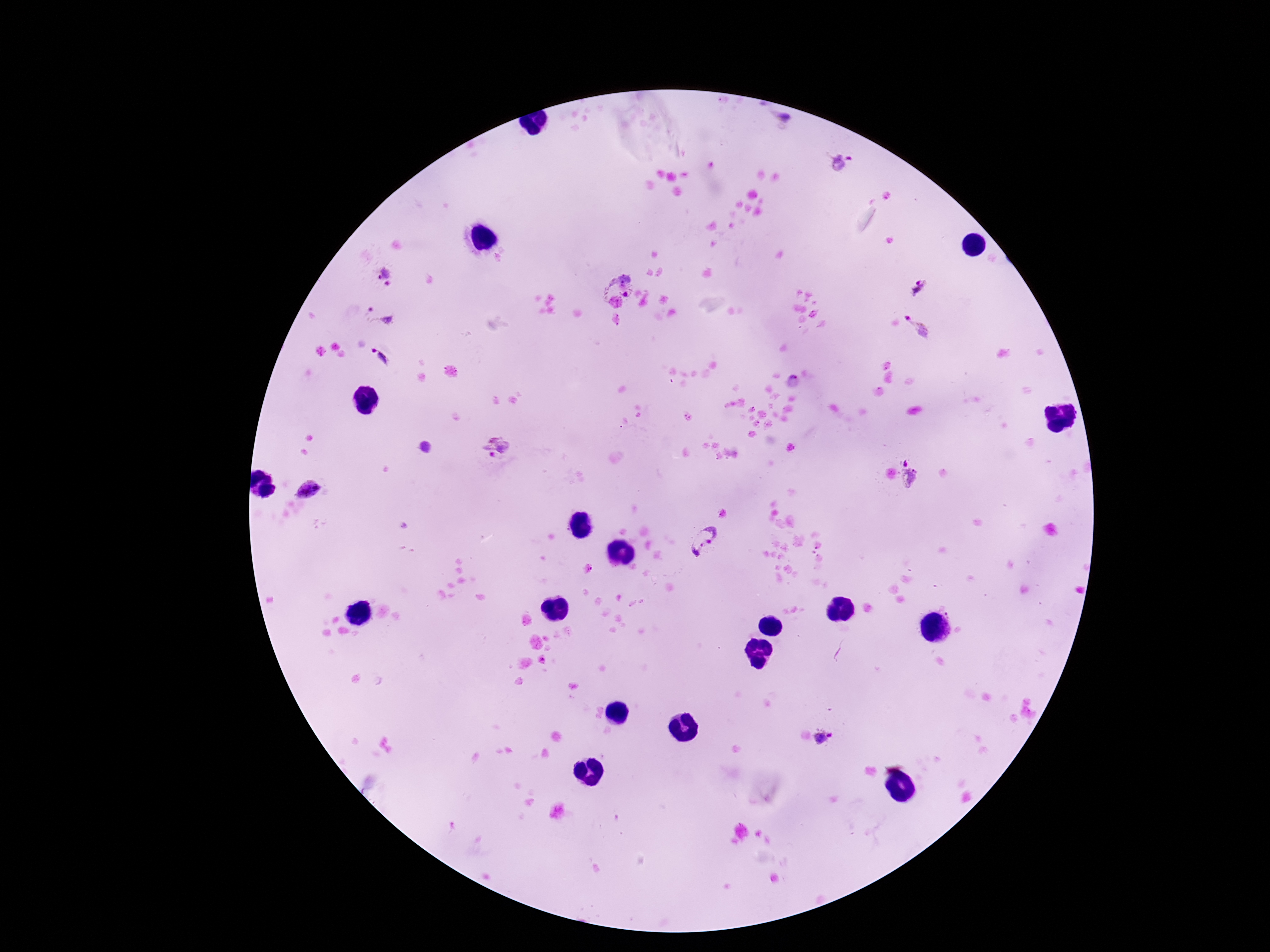
Approximate centers as [x, y] in pixels. Plasmodium parasite locations: [841, 163], [386, 276], [615, 278], [921, 287], [378, 315], [919, 326], [381, 356], [496, 448], [912, 473], [309, 490], [707, 543], [825, 737]. Smartphone photograph taken through the microscope eyepiece. Single field of view. 100x magnification. Image is 1270×952 pixels. Patient malaria status: infected. Giemsa-stained preparation. Thick blood film.